Name the parasite shown.
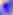
Toxoplasma gondii.

Photomicrograph. Captured at 400x magnification.